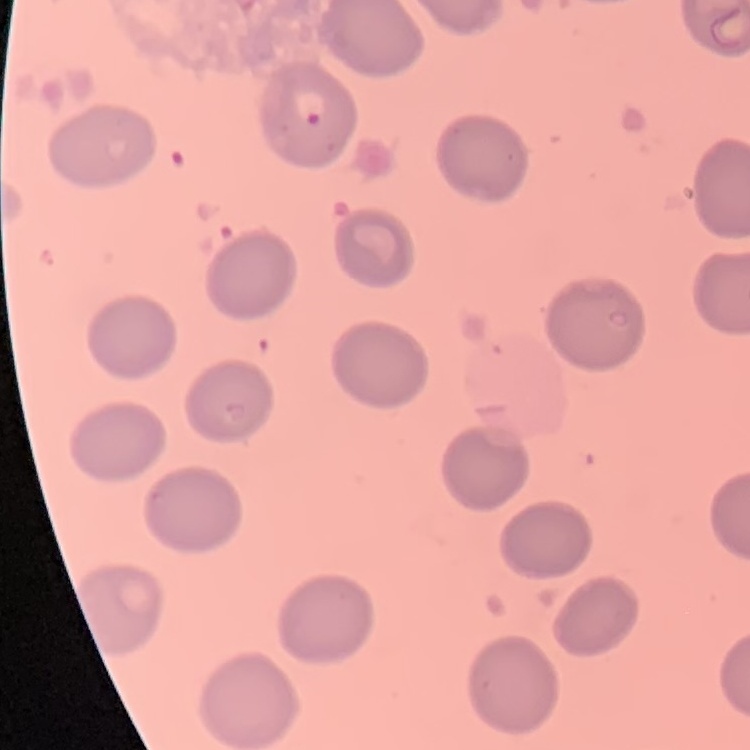
The red blood cells exhibit no rouleaux formation. Stained with either Field's or Giemsa. Square crop of a larger photomicrograph. Thin peripheral smear.